Outline each uninfected red blood cell.
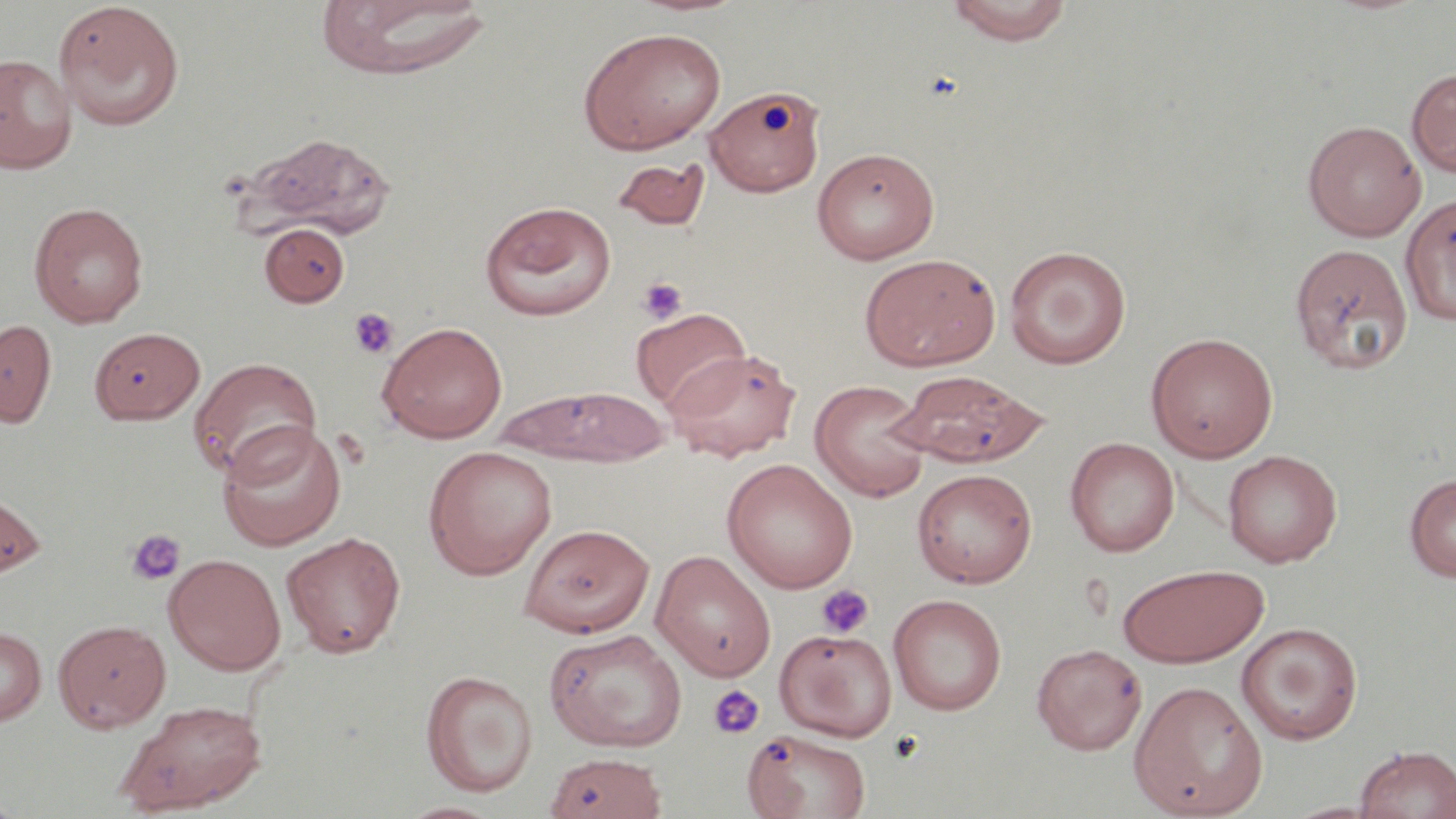
Approximate bounding boxes as named x1/y1/x2/y2 corners in pixels.
Uninfected red blood cells: (x1=315, y1=1, x2=493, y2=81), (x1=943, y1=1, x2=1075, y2=45), (x1=53, y1=3, x2=185, y2=131), (x1=577, y1=27, x2=726, y2=154), (x1=0, y1=53, x2=77, y2=174), (x1=1406, y1=68, x2=1456, y2=178), (x1=704, y1=85, x2=826, y2=197), (x1=1303, y1=119, x2=1426, y2=241), (x1=247, y1=132, x2=398, y2=241), (x1=812, y1=147, x2=940, y2=264), (x1=612, y1=158, x2=711, y2=230), (x1=1400, y1=193, x2=1456, y2=326), (x1=480, y1=201, x2=617, y2=321), (x1=29, y1=202, x2=148, y2=327), (x1=260, y1=222, x2=350, y2=307), (x1=1289, y1=242, x2=1414, y2=374), (x1=1004, y1=245, x2=1132, y2=368), (x1=859, y1=253, x2=1000, y2=372), (x1=631, y1=307, x2=750, y2=412), (x1=0, y1=318, x2=57, y2=427), (x1=377, y1=321, x2=508, y2=443), (x1=88, y1=326, x2=205, y2=424), (x1=1145, y1=332, x2=1279, y2=462), (x1=664, y1=347, x2=801, y2=462), (x1=189, y1=357, x2=324, y2=479), (x1=893, y1=370, x2=1051, y2=468), (x1=810, y1=380, x2=932, y2=502), (x1=496, y1=386, x2=672, y2=466), (x1=216, y1=420, x2=346, y2=550), (x1=1066, y1=437, x2=1180, y2=557), (x1=423, y1=445, x2=558, y2=580), (x1=1222, y1=449, x2=1342, y2=567), (x1=721, y1=458, x2=858, y2=593), (x1=912, y1=468, x2=1037, y2=588), (x1=1404, y1=473, x2=1456, y2=582), (x1=0, y1=488, x2=46, y2=582), (x1=519, y1=522, x2=655, y2=636), (x1=281, y1=531, x2=407, y2=658), (x1=651, y1=550, x2=776, y2=681), (x1=163, y1=553, x2=287, y2=675), (x1=1118, y1=563, x2=1271, y2=668), (x1=888, y1=593, x2=1007, y2=716), (x1=53, y1=618, x2=171, y2=733), (x1=1236, y1=622, x2=1363, y2=744), (x1=0, y1=626, x2=46, y2=725), (x1=544, y1=628, x2=688, y2=752), (x1=775, y1=628, x2=897, y2=741), (x1=1031, y1=643, x2=1147, y2=754), (x1=420, y1=670, x2=538, y2=797), (x1=1129, y1=679, x2=1267, y2=818), (x1=113, y1=699, x2=268, y2=816), (x1=742, y1=728, x2=871, y2=818), (x1=1354, y1=744, x2=1456, y2=819), (x1=544, y1=752, x2=667, y2=819), (x1=395, y1=800, x2=505, y2=818).

Platelet locations: (x1=637, y1=276, x2=688, y2=324), (x1=348, y1=308, x2=399, y2=359), (x1=126, y1=529, x2=187, y2=587), (x1=816, y1=584, x2=874, y2=638), (x1=707, y1=684, x2=765, y2=739). Slide-level diagnosis: negative for blood parasites. May-Grünwald-Giemsa stain. Captured at 1000x magnification. Thin blood smear. Single field of view. Light microscopy. Image is 1456×819 pixels.